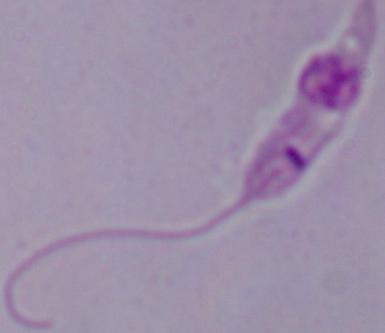 A Leishmania parasite is seen. Photomicrograph. 1000x magnification.